Find the red blood cells that are infected with Plasmodium falciparum, and any of indeterminate infection status.
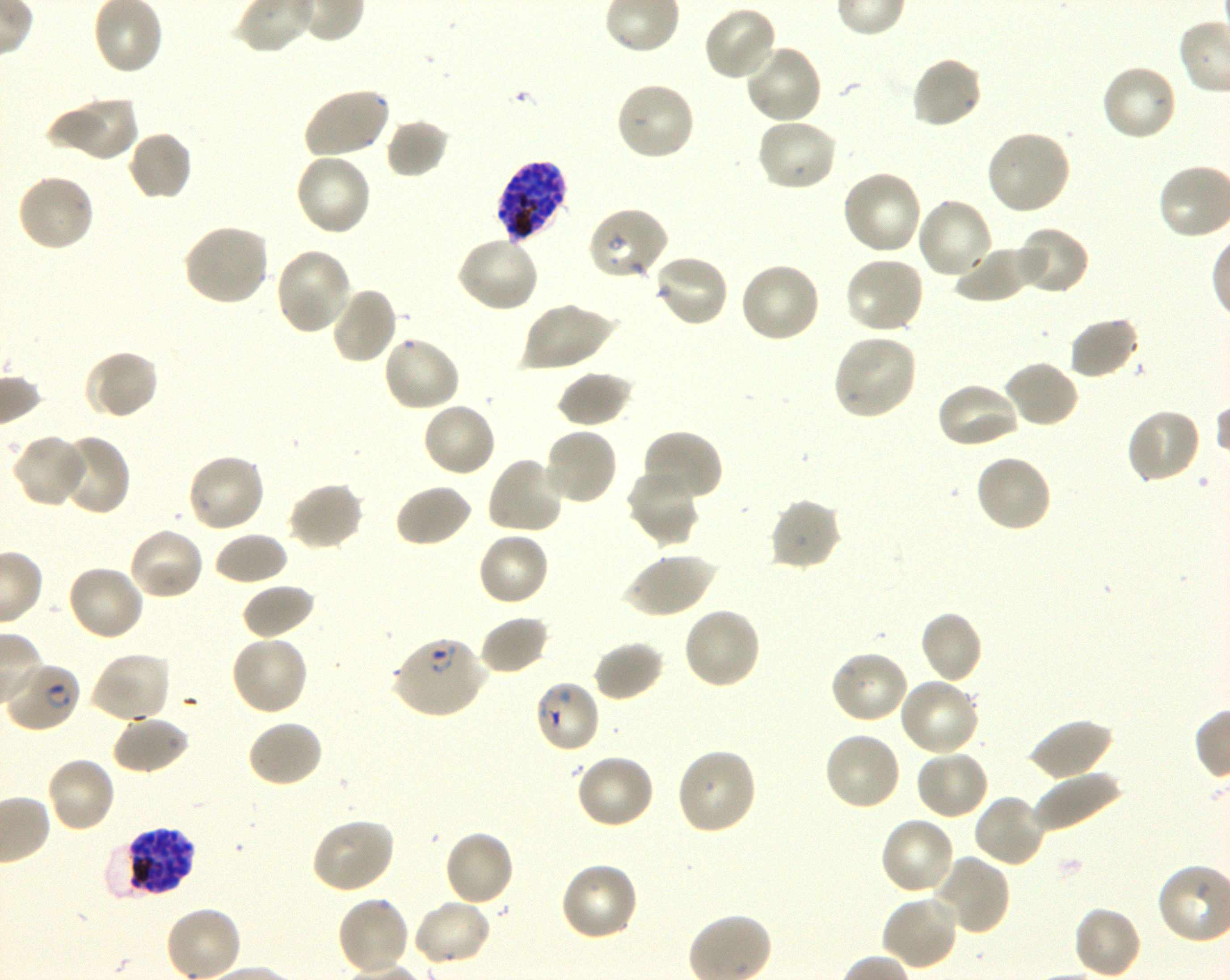

Approximate bounding boxes as (x1, y1, x2, y2) in pixels. Not every red blood cell is marked. A life-cycle stage — or a range of stages, where the recorded stages span more than one — follows each staged infected red blood cell.
Infected red blood cells: (496, 159, 571, 243) schizont; (391, 637, 488, 718) ring; (4, 662, 80, 733) ring; (114, 827, 196, 898) schizont.
Red blood cells of indeterminate infection status: (532, 680, 601, 755).

Locations of uninfected red blood cells: (702, 5, 780, 83), (743, 42, 823, 124), (910, 55, 984, 130), (1100, 63, 1179, 143), (615, 81, 696, 162), (303, 86, 391, 160), (55, 96, 140, 162), (756, 117, 840, 192), (385, 118, 451, 178), (985, 128, 1073, 216), (126, 129, 194, 202), (293, 152, 373, 237), (840, 169, 923, 257), (15, 172, 95, 253), (914, 197, 995, 281), (586, 207, 669, 282), (181, 223, 270, 307), (1014, 226, 1090, 296), (455, 236, 541, 314), (953, 245, 1042, 304), (274, 246, 354, 335), (652, 253, 729, 328), (843, 255, 926, 335), (738, 261, 821, 344), (329, 285, 399, 365), (520, 301, 615, 372), (1068, 316, 1142, 380), (832, 333, 918, 420), (382, 335, 461, 414), (83, 349, 159, 421), (1002, 360, 1079, 430), (556, 371, 632, 427), (934, 381, 1021, 450), (421, 401, 497, 478), (1126, 407, 1202, 485), (542, 426, 619, 507), (640, 428, 723, 505), (54, 434, 131, 515), (12, 435, 86, 508), (186, 453, 267, 534), (973, 454, 1053, 534), (485, 455, 567, 535), (626, 467, 701, 547), (288, 482, 365, 551), (394, 483, 473, 549), (769, 497, 844, 571), (127, 525, 206, 601), (476, 531, 551, 608), (212, 532, 288, 586), (623, 551, 716, 618), (66, 563, 146, 642), (240, 583, 316, 641), (681, 607, 761, 691), (918, 610, 983, 685), (478, 614, 551, 676), (230, 634, 309, 716), (593, 641, 665, 703), (830, 649, 910, 725), (89, 651, 173, 724), (897, 678, 981, 758), (112, 714, 191, 775), (1029, 718, 1115, 782), (246, 719, 324, 789), (822, 731, 901, 812), (675, 747, 758, 836), (914, 749, 991, 820), (574, 752, 656, 829), (44, 756, 118, 833), (1032, 769, 1122, 833), (972, 793, 1047, 868), (878, 816, 956, 898), (310, 818, 396, 895), (443, 829, 515, 907), (931, 855, 1011, 937), (559, 862, 640, 942), (880, 895, 960, 972), (335, 896, 412, 976), (410, 899, 493, 968), (165, 905, 242, 980), (1072, 905, 1142, 980). Life-cycle stages observed: ring, schizont. Thin blood smear. Giemsa-stained preparation. Blood group of the donor: O+. Single field of view. Image is 1230×980 pixels. Plasmodium falciparum strain 3D7 in shaking in-vitro culture. 100x oil-immersion objective, numerical aperture 1.30.